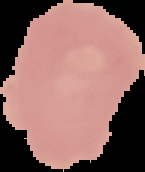

Summary:
  - Image size: 145×172 pixels
  - Malaria status: uninfected
  - Image type: segmented cell region with the area outside set to black
  - Preparation: thin blood film